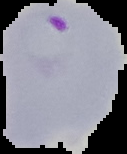

preparation = thin blood smear
malaria status = parasitized
image type = segmented cell region with the area outside set to black
image size = 127×154 pixels